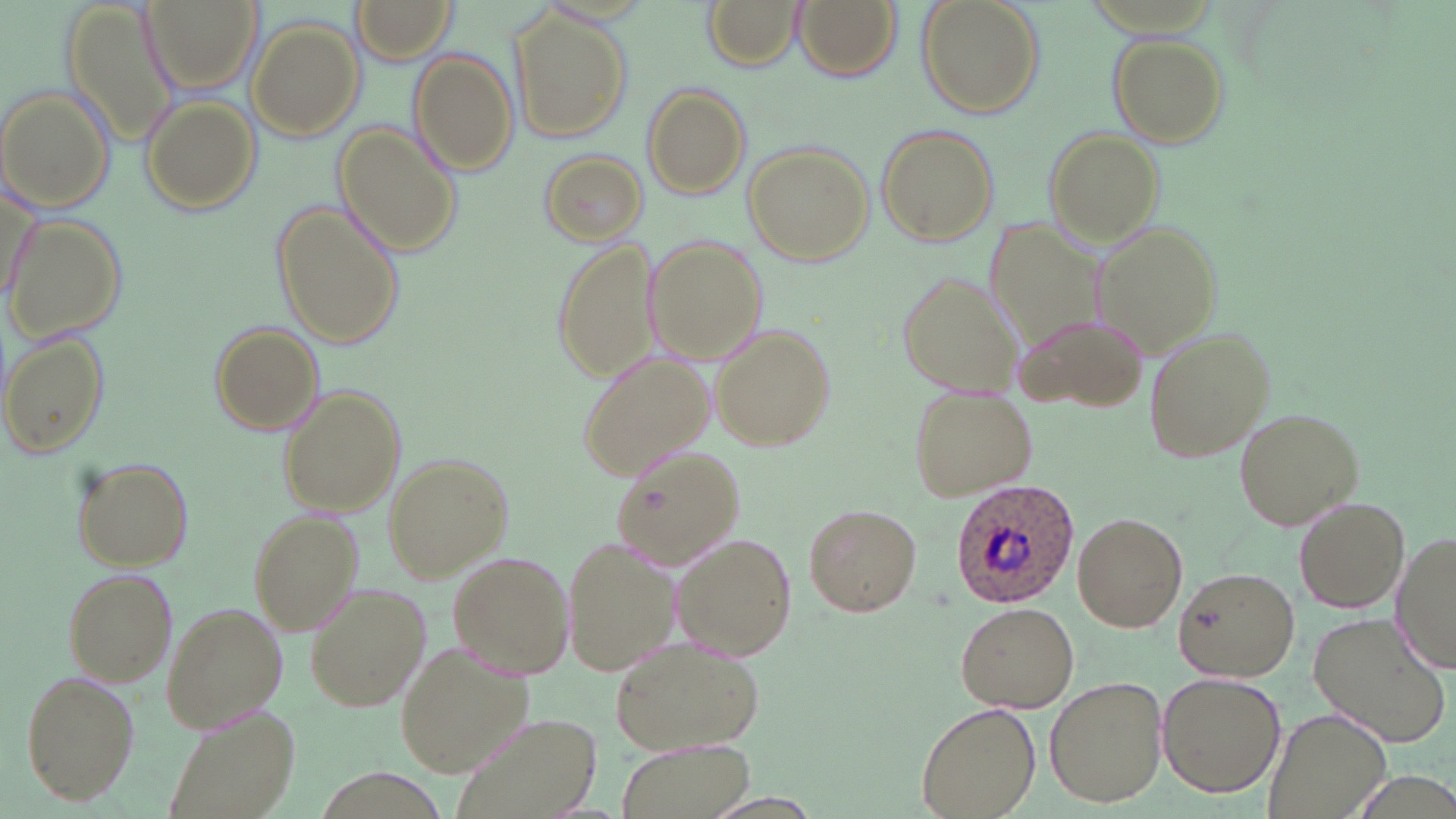

slide_level_diagnosis: Plasmodium ovale
field_of_view: one of a larger specimen
preparation: thin blood film
magnification: 1000x
image_size: 1456×819 pixels
uninfected_red_blood_cell_locations: 'approximate bounding boxes as (x1,y1)-(x2,y2) corner pairs in pixels: (139,0)-(258,94), (350,0)-(462,66), (703,0)-(803,67), (791,0)-(902,81), (917,0)-(1044,116), (513,9)-(631,142), (248,20)-(364,142), (1107,33)-(1230,148), (410,50)-(519,174), (642,83)-(751,198), (0,84)-(116,214), (139,95)-(261,215), (333,123)-(461,257), (873,124)-(1000,247), (1042,128)-(1165,246), (742,141)-(874,268), (538,150)-(649,246), (2,174)-(42,311), (273,202)-(402,348), (982,213)-(1112,359), (3,215)-(127,342), (1090,219)-(1219,358), (645,237)-(767,366), (553,241)-(661,383), (894,267)-(1024,399), (1014,310)-(1151,412), (209,321)-(324,437), (710,324)-(835,449), (1144,325)-(1276,463), (1,333)-(108,459), (578,350)-(718,480), (277,385)-(403,515), (908,385)-(1035,500), (1232,407)-(1362,532), (609,445)-(745,573), (381,454)-(513,580), (74,459)-(193,571), (1291,498)-(1411,614), (804,503)-(922,616), (247,510)-(365,634), (1072,512)-(1188,631), (1393,529)-(1455,676), (562,533)-(681,676), (670,533)-(797,660), (449,551)-(575,680), (60,566)-(178,686), (1172,566)-(1299,681), (305,580)-(431,713), (160,599)-(289,731), (956,601)-(1078,713), (1306,611)-(1453,748), (608,633)-(766,758), (397,640)-(535,776), (20,670)-(140,807), (1158,672)-(1286,797), (1045,676)-(1169,808), (918,701)-(1040,818), (163,703)-(300,819), (449,707)-(605,819), (1264,707)-(1393,819), (620,737)-(755,819)'
stain: May-Grünwald-Giemsa
plasmodium_ovale_infected_red_blood_cell_locations: 'approximate bounding boxes as (x1,y1)-(x2,y2) corner pairs in pixels: (946,478)-(1081,612)'
modality: optical microscopy